Assess the morphology of the erythrocytes.
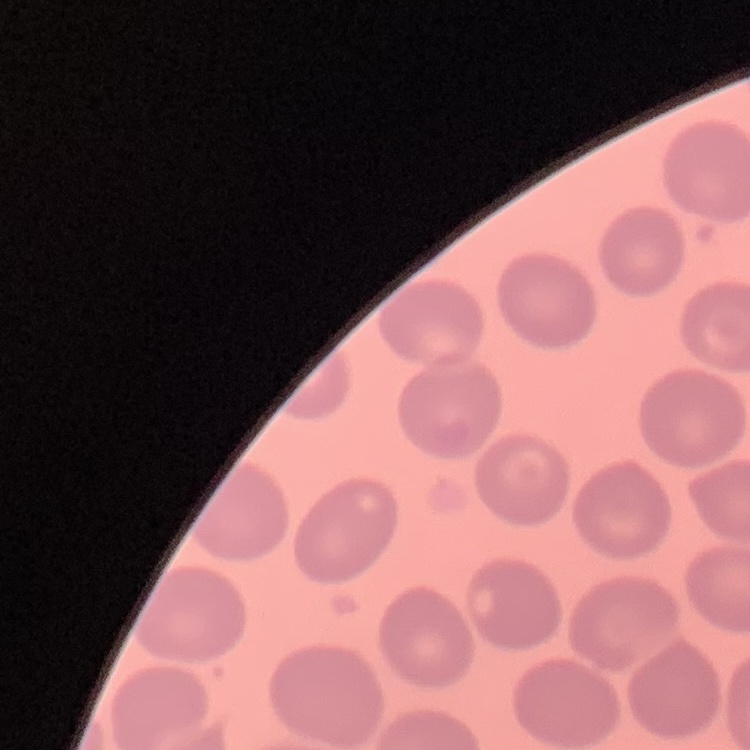
They show no rouleaux formation.

Stained with either Field's or Giemsa. One tile cut from a larger photomicrograph. Thin peripheral smear.